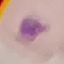

result: negative for malaria parasites
stain: Giemsa
capture: smartphone camera at the microscope eyepiece
preparation: thin blood smear
image_type: cell patch, automatically extracted from a larger field of view and resized to 64 × 64 pixels